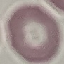
result: negative for malaria parasites
image_type: cell patch, automatically extracted from a larger field of view and resized to 64 × 64 pixels
stain: Giemsa
preparation: thin smear
capture: smartphone camera at the microscope eyepiece